Report the malaria status of this cell.
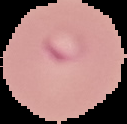

Parasitized.

{
  "image_size": "127×124 pixels",
  "preparation": "thin blood film",
  "image_type": "segmented cell region on a black background"
}